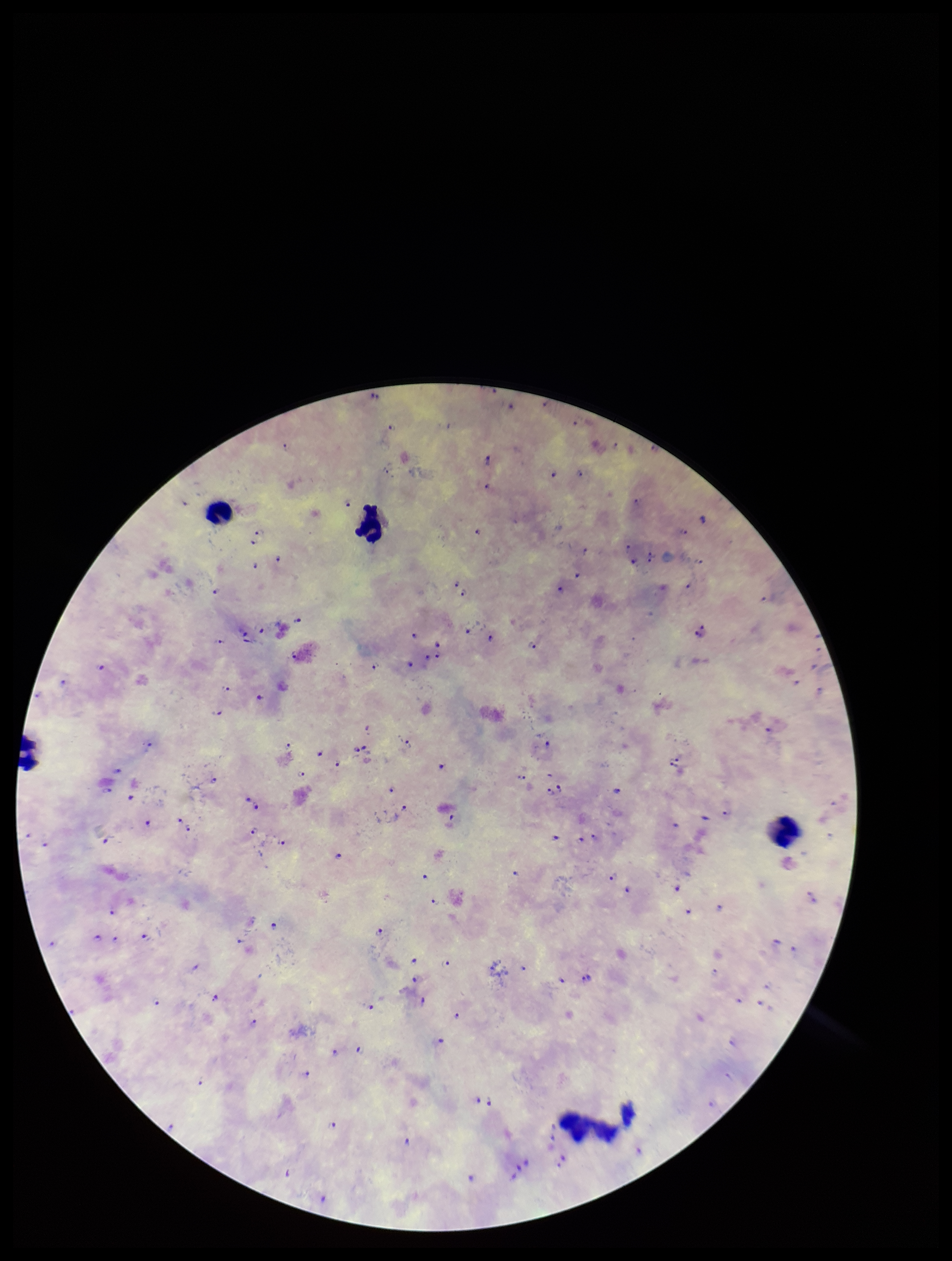
capture = smartphone photograph through the microscope eyepiece
Plasmodium parasites = seen
parasite count = 126
preparation = thick
field of view = single
image size = 952×1261 pixels
stain = Giemsa
leukocyte count = 4
species reported for this patient = Plasmodium falciparum
patient malaria status = positive